State the preparation type.
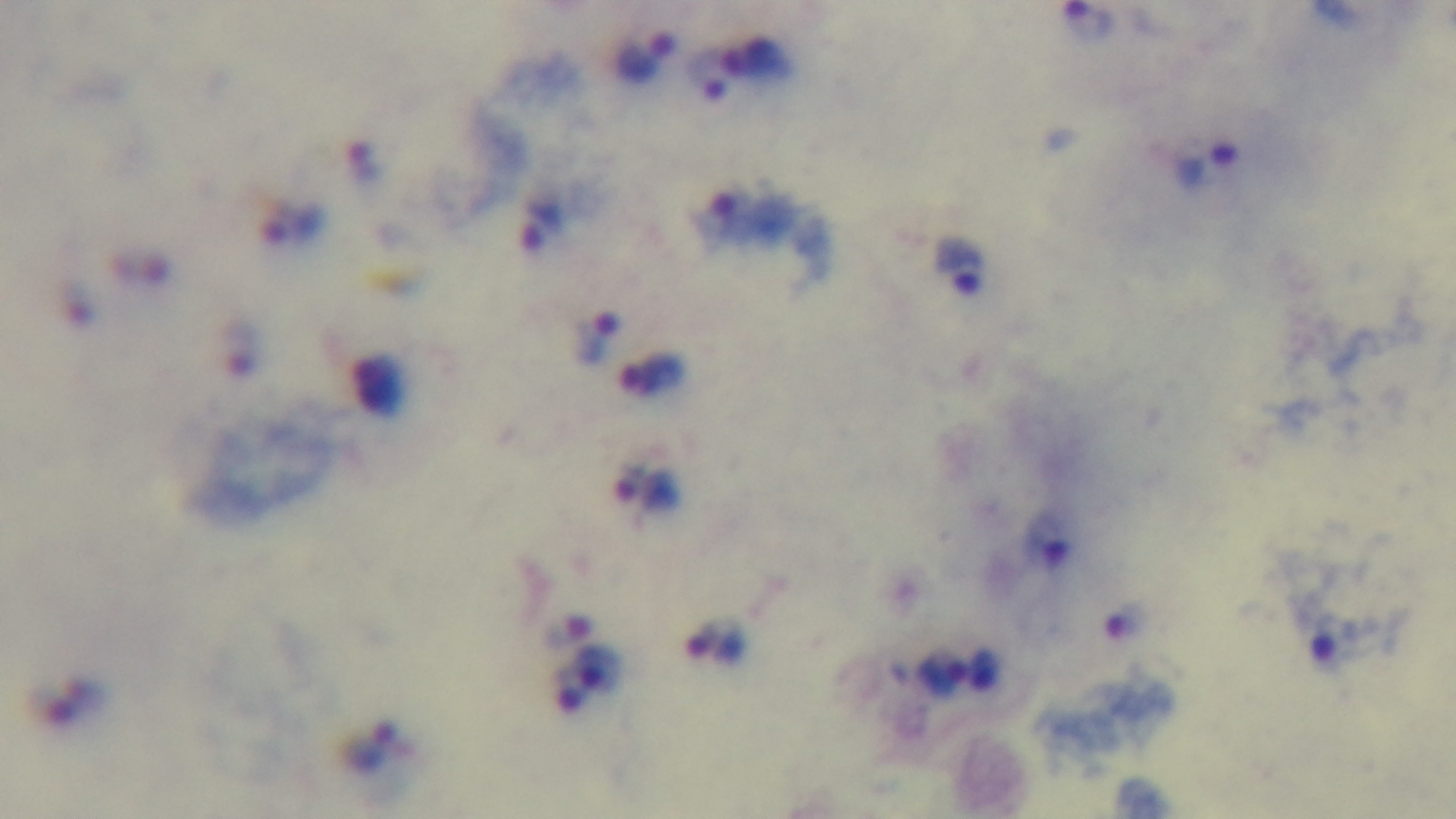
Thick.

Mounted 4K digital camera. Giemsa-stained. Malaria status: infected. Oil-immersion objective, 100x. Photomicrograph. One field from the slide.